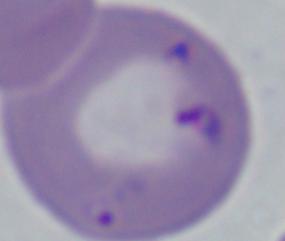

modality = photomicrograph
identification = Babesia
magnification = 1000x